Locate malaria parasites and leukocytes.
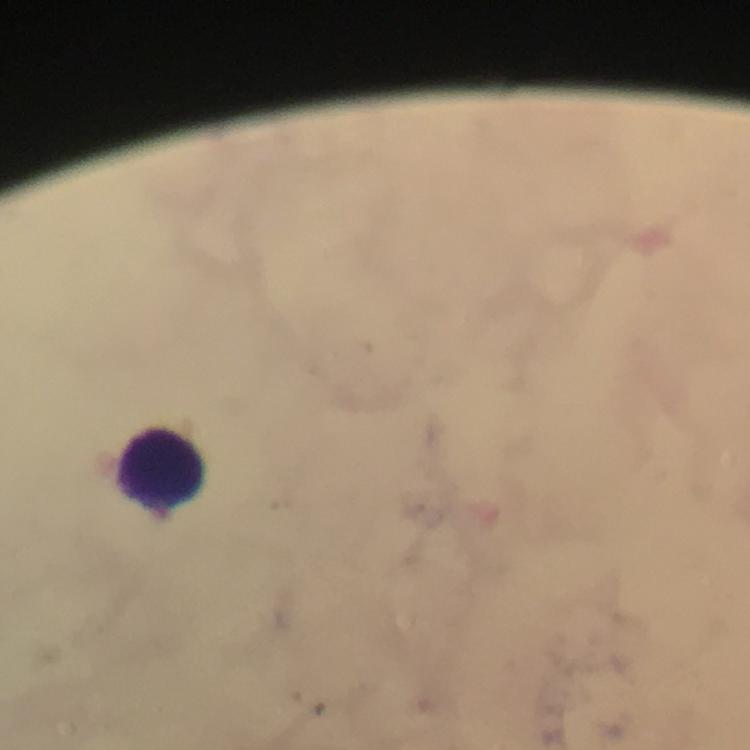
No malaria parasites detected.
Approximate object centers, in pixels from the top-left corner.
Leukocytes: (x=159, y=470).

Summary:
  - Magnification: 100x
  - Capture: smartphone camera through the microscope
  - Cropped from: a single field of view
  - Image size: 750×750 pixels
  - Context: from a diagnostic examination for malaria
  - Immersion oil: applied
  - Preparation: thick blood smear
  - Stain: Giemsa